Report the malaria status of this cell.
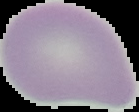

Uninfected.

Image is 139×112 pixels. The area outside the segmented cell region is set to black. From a thin blood film.